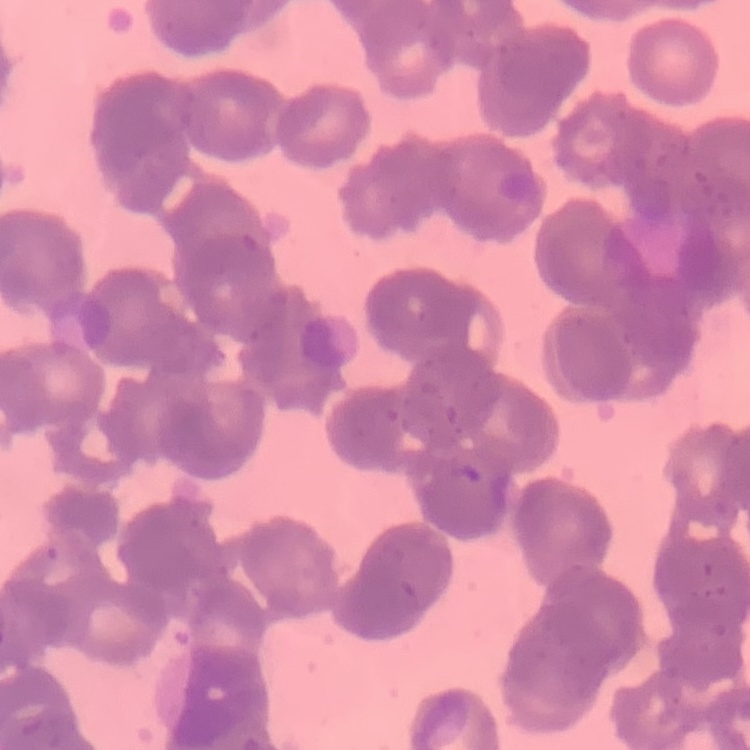
Summary:
  - Erythrocyte morphology: rouleaux formation
  - Preparation: thin blood smear
  - Stain: Field's or Giemsa
  - Image type: one tile cut from a larger photomicrograph